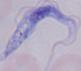

Captured at 1000x magnification. Micrograph. A trypanosome is seen.